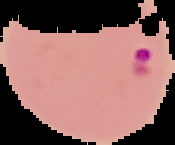 Segmented cell region on a black background. Malaria status: parasitized. Image is 175×145 pixels. From a thin blood smear.